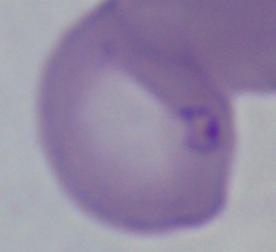

1000x magnification. A Babesia parasite is shown. Micrograph.